Classify this cell by malaria status.
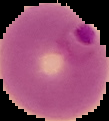
It is parasitized.

image size = 109×121 pixels
preparation = thin blood film
image type = segmented cell region on a black background